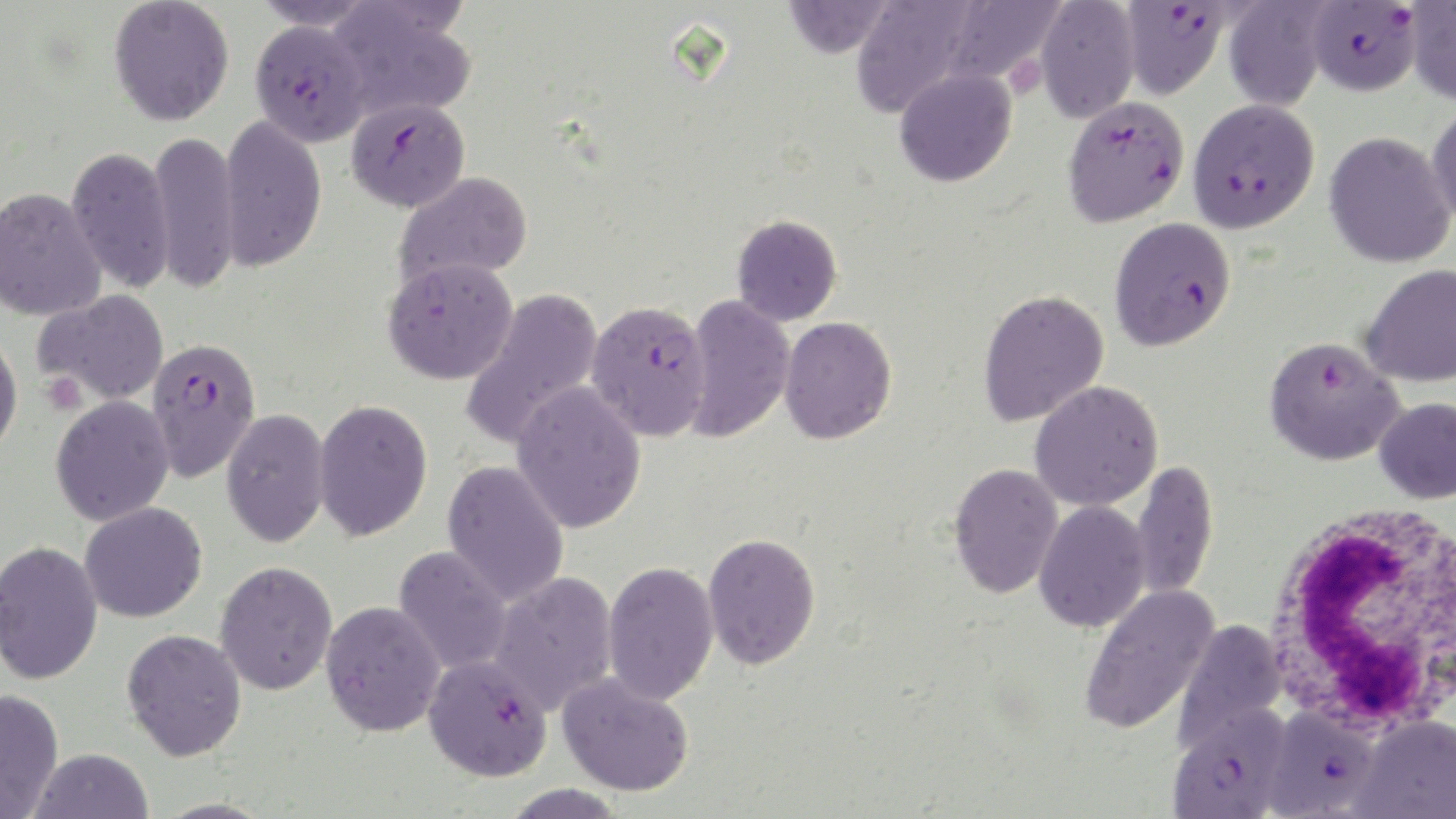

slide-level diagnosis = Plasmodium falciparum
stain = May-Grünwald-Giemsa
preparation = thin blood smear
Plasmodium falciparum-infected red blood cell locations = approximate bounding boxes as (x1, y1, x2, y2) in pixels: (1305, 1, 1422, 96), (1119, 2, 1230, 99), (249, 19, 371, 147), (1063, 95, 1189, 227), (347, 97, 471, 212), (1187, 98, 1319, 233), (1109, 217, 1236, 351), (586, 300, 711, 441), (1264, 336, 1404, 466), (146, 337, 261, 482), (423, 654, 553, 781), (1167, 705, 1291, 819), (1263, 705, 1380, 818)
image size = 1456×819 pixels
modality = optical microscopy
magnification = 1000x
uninfected red blood cell locations = approximate bounding boxes as (x1, y1, x2, y2) in pixels: (108, 0, 234, 126), (251, 0, 378, 30), (782, 0, 895, 58), (850, 0, 980, 119), (939, 0, 1064, 85), (1035, 0, 1140, 124), (325, 1, 476, 122), (1222, 1, 1329, 112), (1405, 2, 1456, 106), (894, 67, 1017, 187), (1427, 101, 1456, 229), (219, 115, 327, 271), (147, 131, 240, 294), (1324, 132, 1455, 269), (65, 146, 175, 293), (393, 171, 533, 290), (0, 187, 107, 321), (731, 213, 842, 326), (382, 256, 518, 384), (1360, 263, 1456, 388), (460, 288, 604, 450), (33, 289, 169, 405), (977, 289, 1109, 427), (681, 294, 795, 443), (779, 316, 897, 444), (0, 329, 23, 459), (1030, 380, 1164, 511), (511, 381, 647, 534), (50, 395, 175, 525), (1375, 396, 1456, 504), (313, 399, 433, 541), (221, 409, 330, 548), (441, 459, 570, 606), (1132, 460, 1219, 601), (948, 462, 1063, 598), (1033, 500, 1151, 632), (79, 502, 207, 623), (702, 532, 821, 670), (0, 540, 103, 685), (393, 546, 513, 675), (215, 560, 338, 695), (601, 560, 719, 706), (487, 571, 617, 716), (1079, 584, 1219, 735), (321, 600, 446, 737), (1174, 619, 1288, 748), (121, 628, 247, 761), (557, 671, 694, 797), (0, 689, 64, 818), (1351, 715, 1456, 819), (28, 747, 153, 819)
white blood cell locations = approximate bounding boxes as (x1, y1, x2, y2) in pixels: (1264, 499, 1455, 734)
field of view = one of a larger specimen